Identify the parasite.
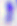

Toxoplasma gondii.

modality: micrograph
magnification: 400x